Locate every leukocyte (white blood cell).
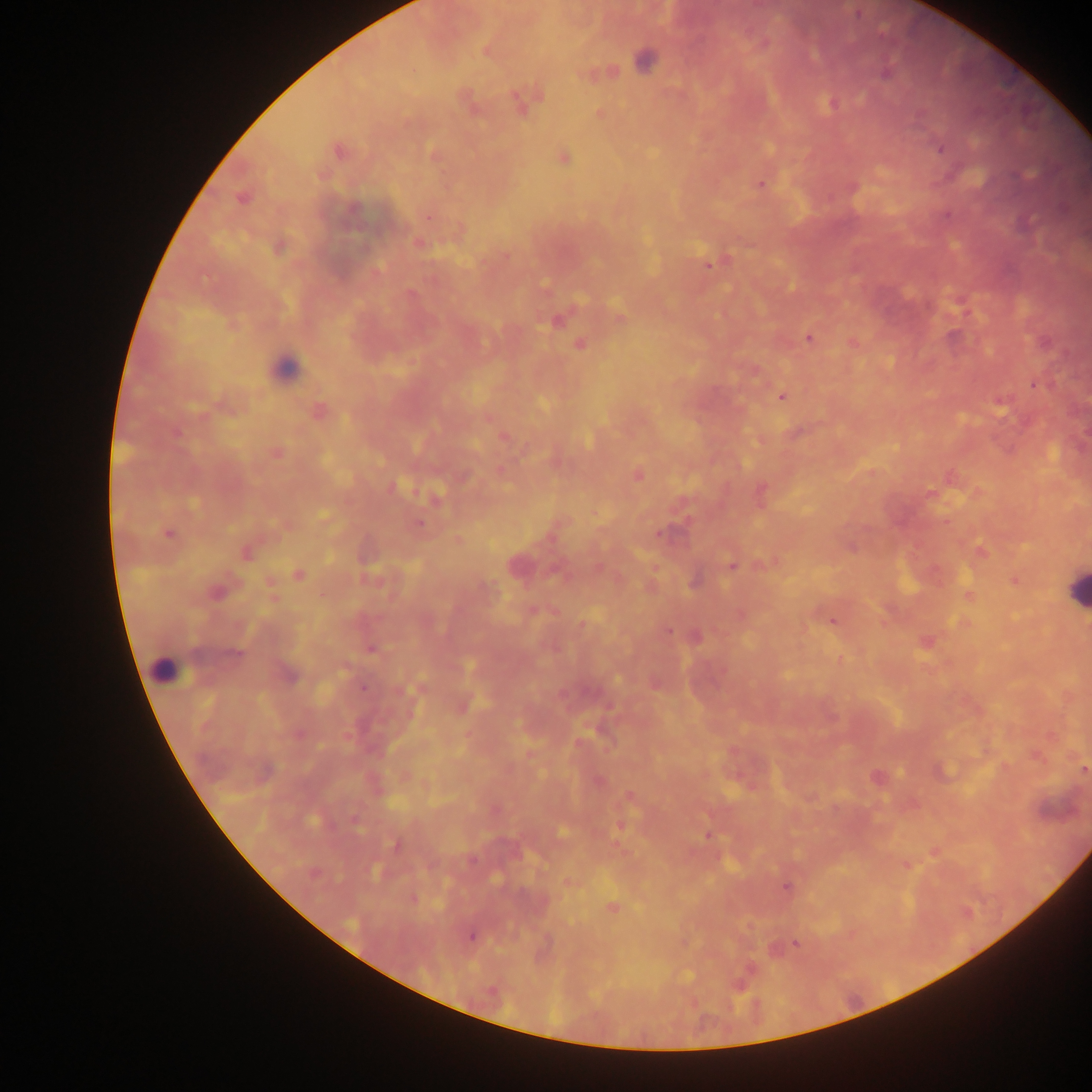

Approximate centers as x y in pixels.
Leukocytes: 285 367; 1075 589; 162 670.

capture = mobile-phone photograph through a microscope
image size = 1092×1092 pixels
country = Ghana
field of view = single
preparation = thick blood smear
Plasmodium parasite locations = approximate centers as x y in pixels: 857 14; 487 51; 644 61; 886 74; 519 103; 832 103; 940 148; 338 151; 563 157; 1018 176; 760 183; 243 198; 419 243; 709 264; 410 293; 556 321; 951 336; 809 339; 580 344; 1034 385; 782 397; 318 411; 504 437; 277 453; 638 475; 761 491; 929 493; 419 525; 169 533; 659 533; 246 554; 731 566; 299 574; 1015 580; 217 592; 832 621; 668 632; 695 637; 371 648; 234 655; 290 676; 363 688; 1083 771; 313 820; 356 821; 563 832; 708 835; 396 844; 473 860; 375 871; 315 874; 786 887; 612 907; 471 936; 796 943